Name the parasite shown.
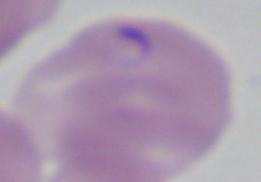

Babesia.

{
  "magnification": "1000x",
  "modality": "photomicrograph"
}